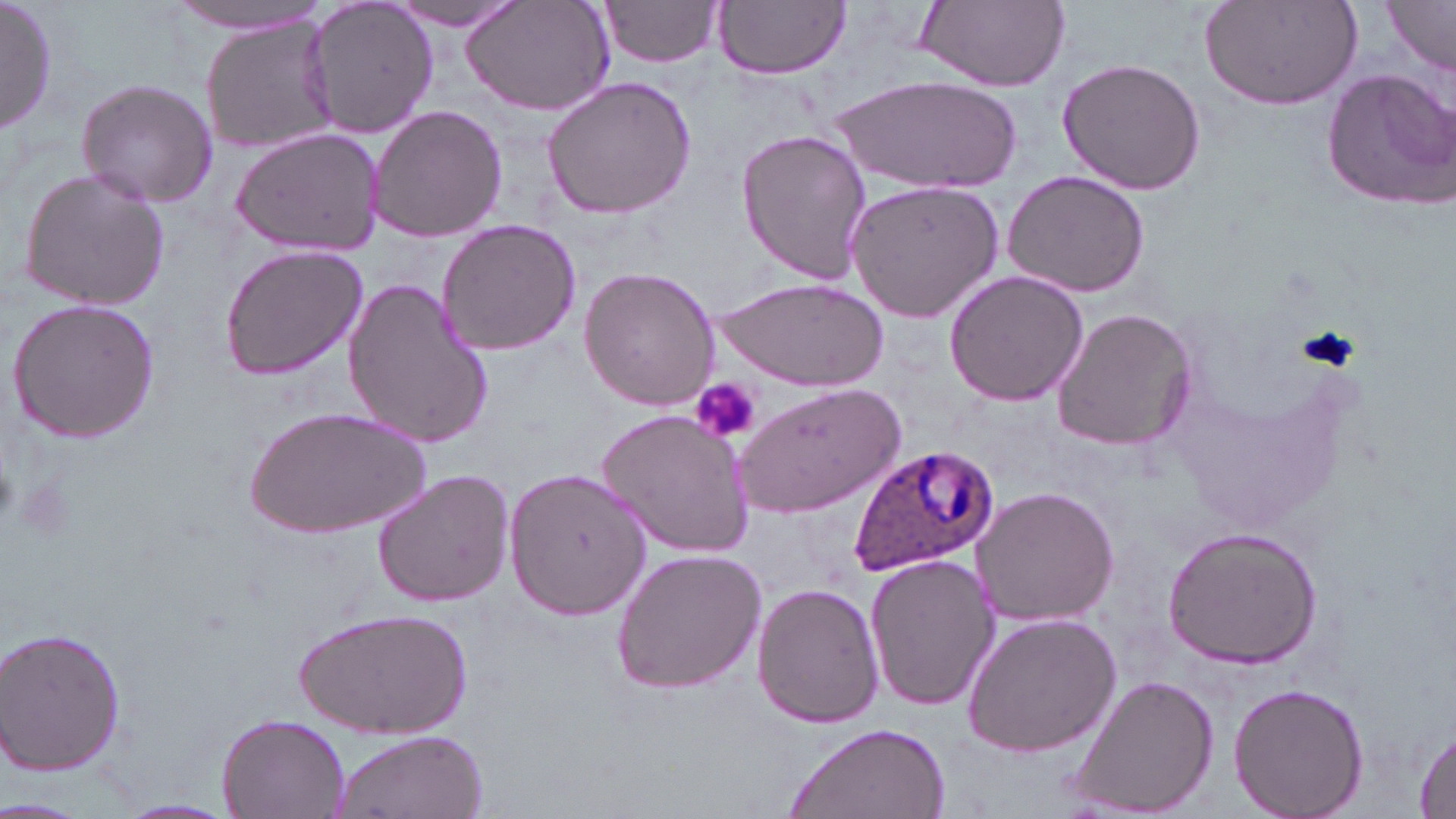

Approximate bounding boxes as named x1/y1/x2/y2 corners in pixels. Platelet locations: (x1=1296, y1=325, x2=1360, y2=372), (x1=693, y1=379, x2=761, y2=443), (x1=0, y1=459, x2=20, y2=526), (x1=16, y1=478, x2=76, y2=543). Plasmodium ovale-infected red blood cell locations: (x1=846, y1=442, x2=1000, y2=578). Uninfected red blood cell locations: (x1=1, y1=0, x2=57, y2=138), (x1=458, y1=0, x2=617, y2=116), (x1=599, y1=0, x2=726, y2=68), (x1=715, y1=0, x2=850, y2=80), (x1=915, y1=0, x2=1070, y2=90), (x1=1199, y1=0, x2=1367, y2=111), (x1=163, y1=1, x2=329, y2=36), (x1=301, y1=1, x2=440, y2=140), (x1=390, y1=1, x2=525, y2=36), (x1=1385, y1=1, x2=1456, y2=73), (x1=200, y1=15, x2=339, y2=156), (x1=1056, y1=58, x2=1208, y2=196), (x1=1321, y1=66, x2=1456, y2=210), (x1=835, y1=74, x2=1025, y2=191), (x1=540, y1=75, x2=698, y2=221), (x1=74, y1=77, x2=219, y2=209), (x1=366, y1=104, x2=508, y2=243), (x1=230, y1=125, x2=385, y2=255), (x1=736, y1=129, x2=873, y2=284), (x1=16, y1=167, x2=171, y2=311), (x1=1002, y1=171, x2=1151, y2=297), (x1=843, y1=180, x2=1005, y2=324), (x1=435, y1=219, x2=584, y2=357), (x1=218, y1=243, x2=370, y2=381), (x1=578, y1=267, x2=721, y2=411), (x1=943, y1=269, x2=1089, y2=407), (x1=341, y1=276, x2=495, y2=450), (x1=716, y1=276, x2=888, y2=389), (x1=7, y1=298, x2=161, y2=443), (x1=1053, y1=306, x2=1197, y2=451), (x1=732, y1=380, x2=907, y2=518), (x1=250, y1=404, x2=429, y2=541), (x1=595, y1=408, x2=756, y2=559), (x1=504, y1=465, x2=653, y2=620), (x1=372, y1=469, x2=517, y2=609), (x1=972, y1=486, x2=1118, y2=626), (x1=1161, y1=526, x2=1324, y2=669), (x1=608, y1=547, x2=768, y2=696), (x1=864, y1=553, x2=998, y2=713), (x1=751, y1=583, x2=884, y2=729), (x1=301, y1=606, x2=467, y2=738), (x1=959, y1=613, x2=1122, y2=758), (x1=2, y1=625, x2=128, y2=776), (x1=1068, y1=677, x2=1219, y2=816), (x1=1228, y1=682, x2=1368, y2=819), (x1=216, y1=710, x2=350, y2=819), (x1=784, y1=721, x2=952, y2=819), (x1=1412, y1=722, x2=1456, y2=819), (x1=327, y1=728, x2=487, y2=819), (x1=116, y1=797, x2=238, y2=818), (x1=0, y1=798, x2=85, y2=819). Slide-level diagnosis: Plasmodium ovale. Optical microscopy. Captured at 1000x magnification. Image is 1456×819 pixels. One field of a larger specimen. May-Grünwald-Giemsa-stained preparation. Thin blood smear.